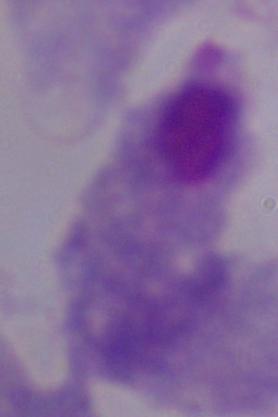
Summary:
  - Magnification: 1000x
  - Identification: trichomonad
  - Modality: photomicrograph